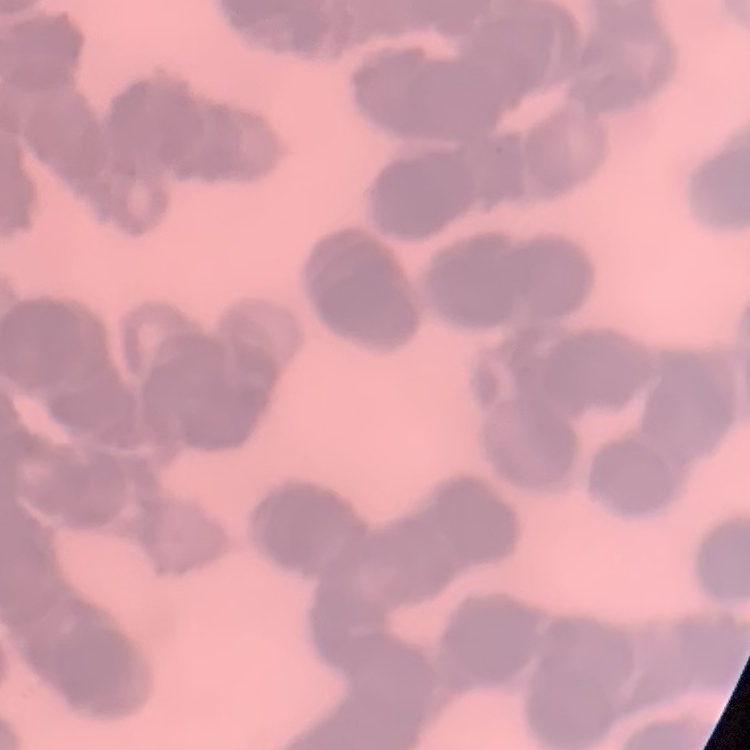 The red blood cells show rouleaux formation. Thin blood film. Square crop of a larger photomicrograph. Stained with either Field's or Giemsa.